Locate every uninfected red blood cell.
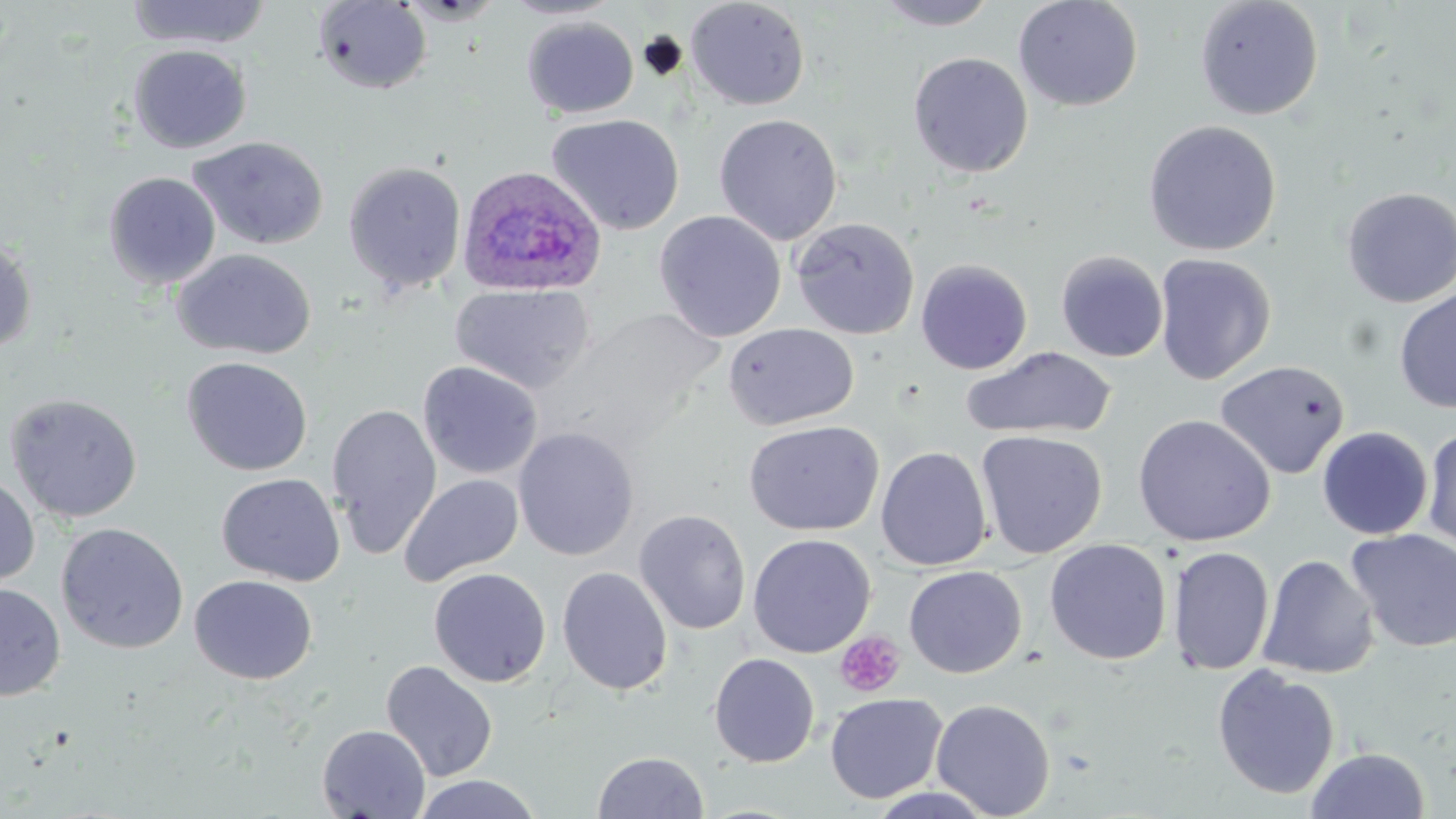

Approximate bounding boxes as (x1,y1)-(x2,y2) corner pairs in pixels.
Uninfected red blood cells: (125,0)-(273,49), (499,0)-(623,20), (685,0)-(811,111), (1013,0)-(1144,112), (1194,0)-(1324,121), (312,1)-(432,94), (872,1)-(1002,30), (522,16)-(639,118), (127,44)-(252,153), (908,51)-(1033,178), (546,113)-(685,235), (713,113)-(843,245), (1143,119)-(1282,256), (187,135)-(330,250), (343,161)-(467,293), (103,171)-(221,289), (1340,186)-(1456,308), (654,210)-(787,342), (791,216)-(920,340), (0,238)-(37,355), (172,248)-(317,360), (1055,250)-(1168,362), (1153,253)-(1276,385), (916,258)-(1032,375), (450,283)-(595,394), (1394,288)-(1456,414), (723,322)-(860,431), (961,346)-(1117,441), (181,356)-(313,476), (1214,359)-(1350,480), (418,361)-(543,481), (4,392)-(143,523), (327,402)-(442,559), (1132,413)-(1276,546), (744,420)-(884,536), (513,426)-(639,561), (1317,426)-(1433,540), (1421,426)-(1456,556), (975,429)-(1108,559), (875,445)-(992,571), (216,472)-(345,586), (398,473)-(524,586), (0,475)-(40,588), (634,509)-(751,635), (631,518)-(876,639), (55,522)-(189,654), (1345,528)-(1456,654), (748,533)-(876,658), (1044,538)-(1172,665), (1168,545)-(1274,676), (1257,554)-(1379,680), (904,565)-(1027,678), (557,566)-(673,696), (428,567)-(552,687), (190,574)-(317,684), (0,583)-(65,701), (708,652)-(820,768), (380,660)-(498,782), (1211,664)-(1341,800), (825,692)-(948,804), (931,698)-(1056,817), (317,724)-(430,818), (1306,747)-(1430,819), (592,750)-(709,818), (413,774)-(541,819).

{
  "slide_level_diagnosis": "Plasmodium ovale",
  "image_size": "1456×819 pixels",
  "preparation": "thin blood smear",
  "stain": "May-Grünwald-Giemsa",
  "plasmodium_ovale_infected_red_blood_cell_locations": "approximate bounding boxes as (x1,y1)-(x2,y2) corner pairs in pixels: (456,164)-(607,298)",
  "modality": "optical microscopy",
  "platelet_locations": "approximate bounding boxes as (x1,y1)-(x2,y2) corner pairs in pixels: (835,630)-(905,698)",
  "magnification": "1000x",
  "field_of_view": "single"
}